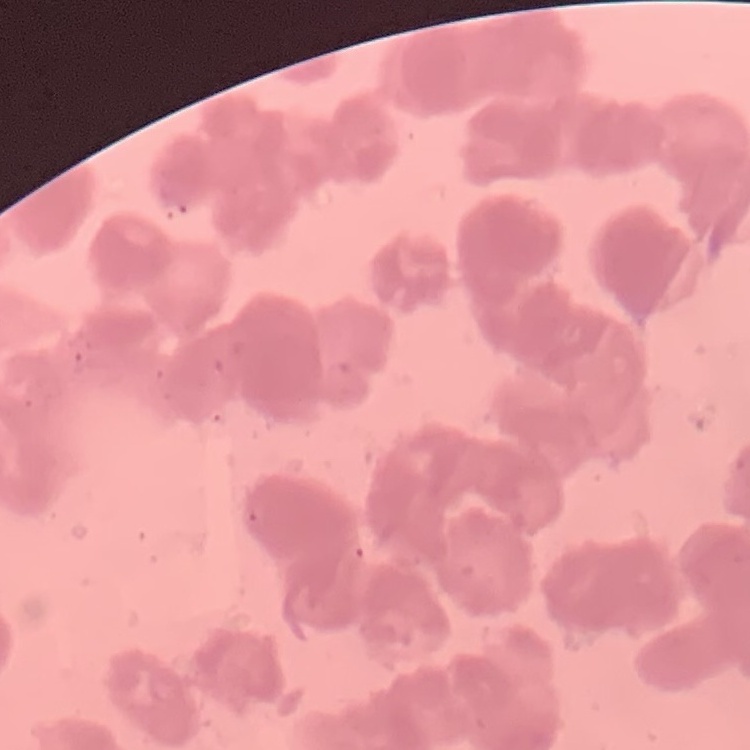

red_blood_cell_morphology: rouleaux formation
stain: Field's or Giemsa
image_type: square crop of a larger photomicrograph
preparation: thin blood film